Assess this cell for malaria.
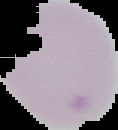

It is uninfected.

image type = segmented cell region with the area outside set to black
preparation = thin blood smear
image size = 118×130 pixels